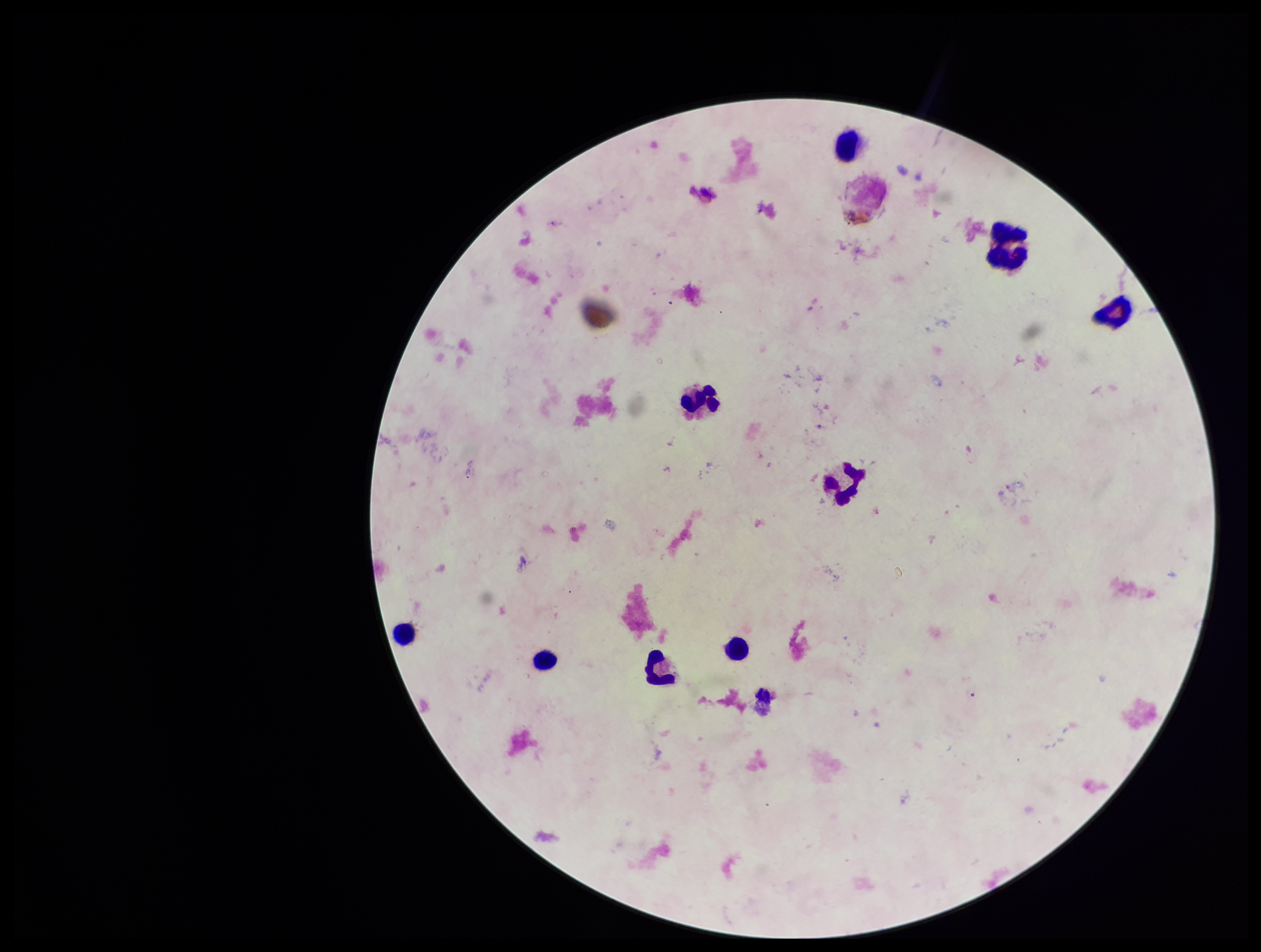
stain: Giemsa
image_size: 1261×952 pixels
patient_malaria_status: negative
plasmodium_parasites: none identified
capture: smartphone photograph through the microscope eyepiece
preparation: thick blood smear
field_of_view: single
parasite_count: 0
leukocyte_count: 9